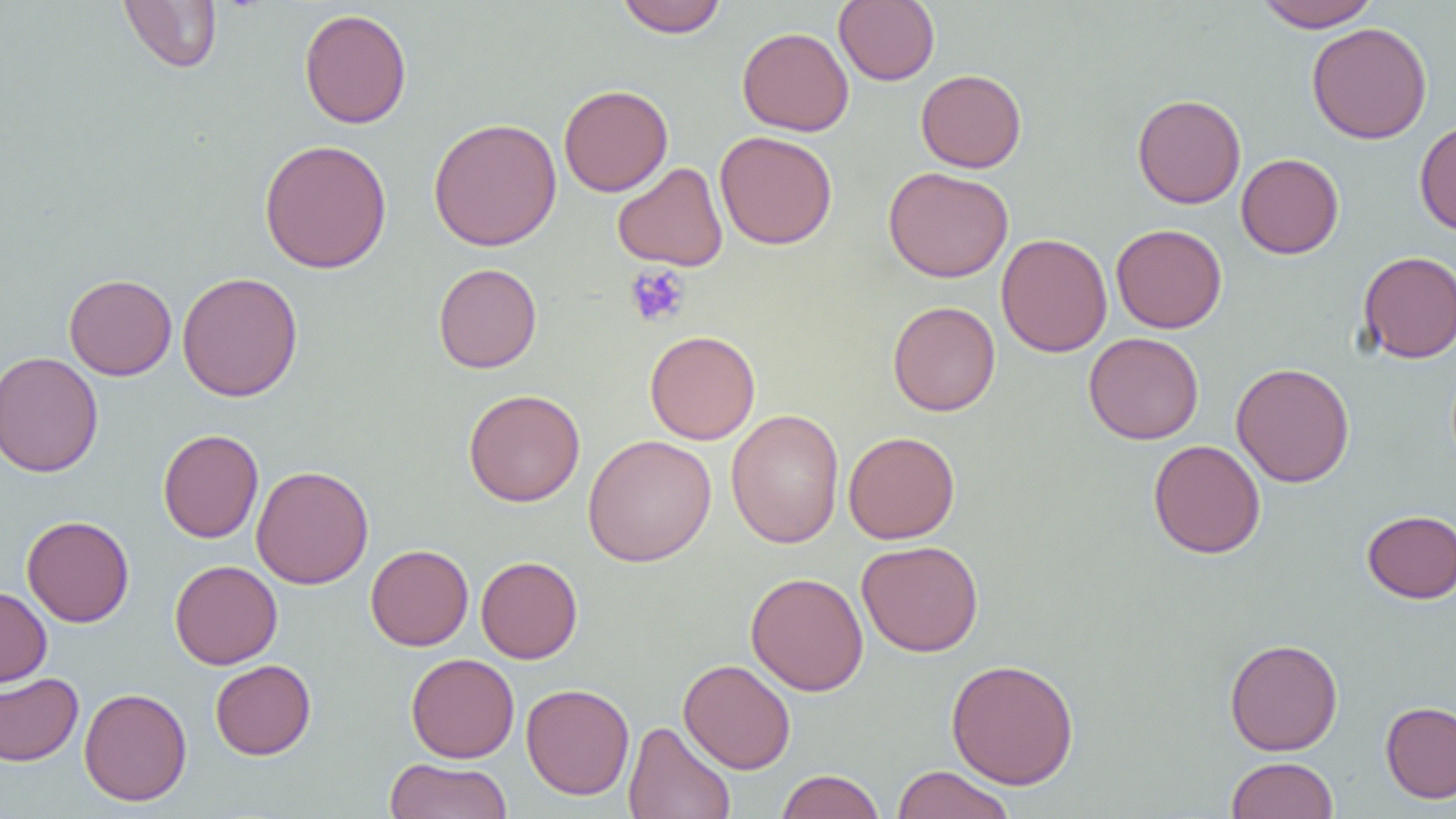
Summary:
  - Coordinate format: approximate bounding boxes as (x1, y1, x2, y2) in pixels
  - Platelet locations: (624, 265, 690, 327)
  - Uninfected red blood cell locations: (616, 0, 728, 38), (834, 0, 940, 86), (1253, 0, 1380, 31), (119, 1, 222, 73), (298, 7, 412, 129), (1306, 22, 1433, 144), (737, 27, 854, 136), (915, 69, 1027, 173), (559, 84, 673, 197), (1132, 93, 1246, 209), (428, 117, 562, 252), (1414, 119, 1456, 237), (715, 131, 837, 250), (259, 139, 392, 273), (1236, 153, 1344, 259), (613, 161, 728, 271), (883, 166, 1013, 283), (1111, 223, 1227, 333), (996, 233, 1112, 357), (1357, 250, 1456, 363), (433, 263, 542, 373), (176, 271, 303, 401), (64, 273, 177, 380), (887, 301, 1000, 416), (645, 329, 761, 444), (1084, 332, 1204, 444), (0, 351, 103, 478), (1231, 362, 1355, 487), (463, 389, 585, 507), (726, 409, 845, 549), (158, 429, 263, 543), (843, 431, 960, 544), (583, 434, 717, 567), (1148, 440, 1265, 559), (251, 465, 374, 589), (1362, 509, 1456, 603), (22, 515, 134, 627), (856, 540, 984, 657), (365, 544, 473, 651), (475, 555, 583, 663), (169, 560, 283, 669), (746, 572, 869, 696), (0, 586, 52, 686), (1224, 638, 1343, 755), (405, 653, 520, 763), (945, 658, 1080, 789), (210, 659, 316, 760), (678, 659, 795, 774), (0, 672, 84, 766), (521, 683, 634, 800), (79, 687, 192, 806), (1380, 701, 1456, 803), (623, 720, 736, 819), (1226, 756, 1338, 819), (383, 758, 513, 819), (890, 765, 1016, 819), (775, 769, 885, 819)
  - Slide-level diagnosis: negative for blood parasites
  - Field of view: single
  - Image size: 1456×819 pixels
  - Preparation: thin blood film
  - Magnification: 1000x
  - Modality: optical microscopy